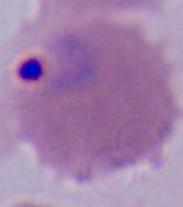

Micrograph. 400x or 1000x magnification. A Plasmodium parasite is seen.